Locate and identify every blood parasite.
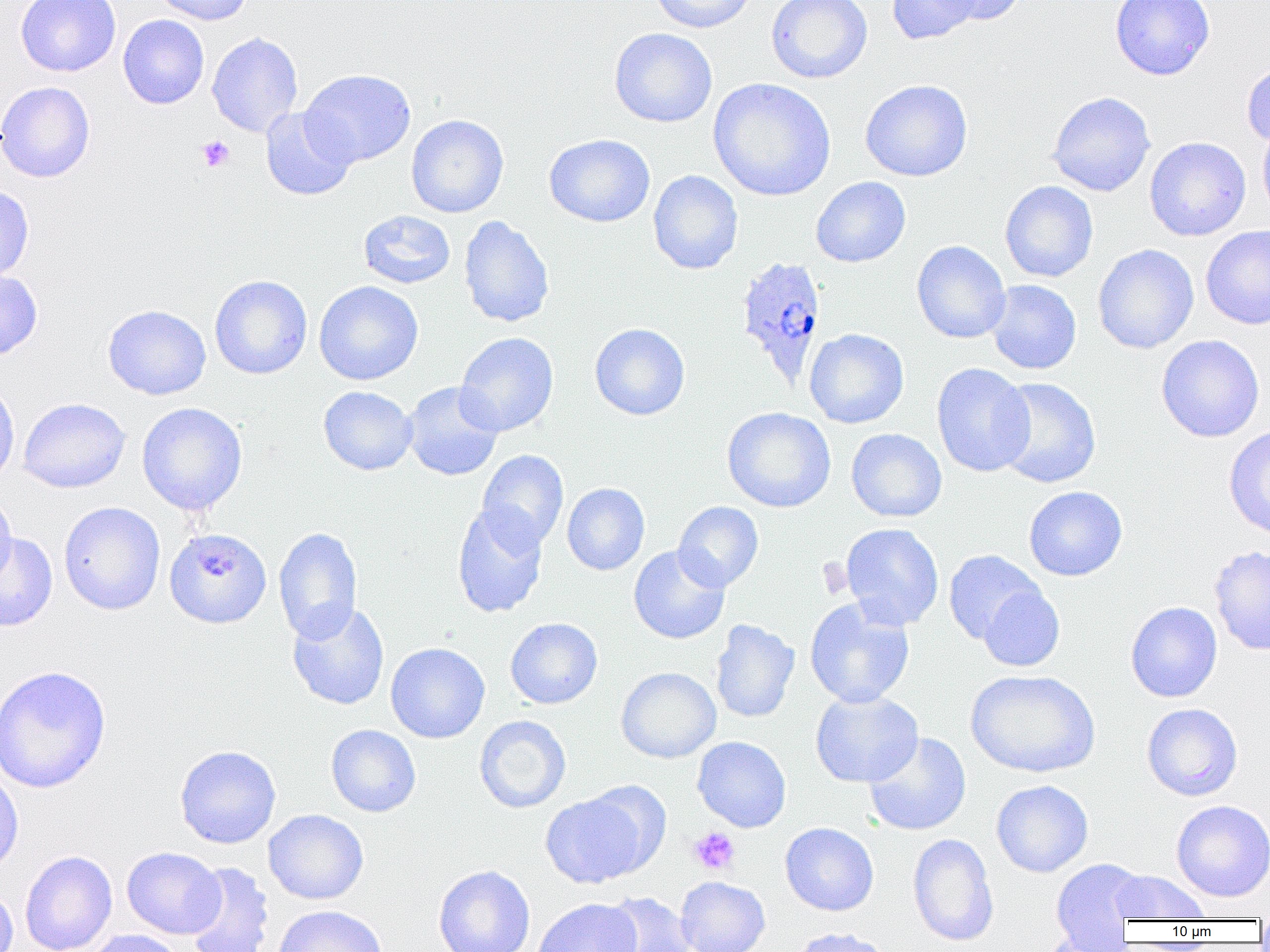

Approximate bounding boxes as (x1,y1)-(x2,y2) corner pairs in pixels.
Plasmodium ovale-infected red blood cells: (734,255)-(827,387).
No Plasmodium falciparum, Plasmodium malariae, Plasmodium vivax, Babesia divergens, or Trypanosoma brucei observed.

Summary:
  - Uninfected red blood cell locations: (15,0)-(121,77), (150,0)-(254,25), (648,0)-(758,33), (766,0)-(872,83), (887,0)-(983,45), (932,0)-(1027,25), (1110,0)-(1215,80), (118,15)-(209,109), (609,28)-(718,127), (207,32)-(303,137), (1241,60)-(1270,148), (300,69)-(416,168), (708,78)-(836,202), (860,79)-(973,182), (0,81)-(95,183), (1047,91)-(1156,197), (260,106)-(357,201), (406,114)-(508,218), (1257,120)-(1270,224), (544,134)-(655,227), (1144,136)-(1251,241), (648,170)-(744,274), (811,176)-(911,268), (1000,181)-(1098,282), (0,185)-(34,283), (358,210)-(456,289), (458,215)-(555,328), (1201,224)-(1270,331), (911,240)-(1011,344), (1092,244)-(1199,354), (0,269)-(43,360), (210,275)-(312,379), (986,280)-(1082,374), (313,281)-(423,386), (103,304)-(211,400), (589,323)-(690,420), (804,328)-(909,428), (455,332)-(558,437), (1155,335)-(1265,442), (931,362)-(1035,477), (993,377)-(1101,488), (0,380)-(20,488), (402,381)-(504,481), (318,386)-(418,475), (18,398)-(131,493), (137,402)-(248,516), (722,407)-(836,513), (1224,425)-(1270,539), (846,428)-(946,522), (477,449)-(569,551), (562,483)-(650,575), (1024,486)-(1127,581), (0,490)-(17,586), (59,501)-(165,615), (452,501)-(548,618), (673,501)-(764,592), (840,523)-(944,630), (273,526)-(363,644), (164,527)-(272,628), (0,532)-(58,632), (628,544)-(730,644), (1209,544)-(1270,656), (943,550)-(1045,644), (978,585)-(1065,672), (804,598)-(915,708), (287,601)-(390,711), (1125,601)-(1223,702), (505,617)-(602,708), (710,619)-(800,723), (385,642)-(490,743), (0,664)-(111,793), (616,667)-(721,763), (965,669)-(1101,778), (810,690)-(923,787), (1141,702)-(1243,801), (474,715)-(571,813), (326,724)-(421,817), (863,732)-(972,836), (692,736)-(792,832), (174,745)-(281,848), (0,768)-(23,876), (991,780)-(1093,878), (540,791)-(651,888), (1171,800)-(1270,902), (263,809)-(368,904), (780,822)-(879,916), (907,833)-(1000,946), (121,847)-(225,938), (19,850)-(118,952), (1049,859)-(1148,948), (183,862)-(274,952), (433,864)-(535,952), (1109,870)-(1209,922), (675,876)-(770,952), (0,883)-(18,952), (599,892)-(696,952), (533,897)-(641,952), (273,904)-(388,952), (790,927)-(893,952), (83,929)-(184,952), (1035,932)-(1133,952)
  - Platelet locations: (196,135)-(234,172), (194,555)-(238,580), (688,826)-(740,875)
  - Slide-level diagnosis: Plasmodium ovale
  - Modality: light microscopy
  - Field of view: single
  - Preparation: thin blood smear
  - Magnification: 1000x
  - Image size: 1270×952 pixels